Locate and identify every blood parasite.
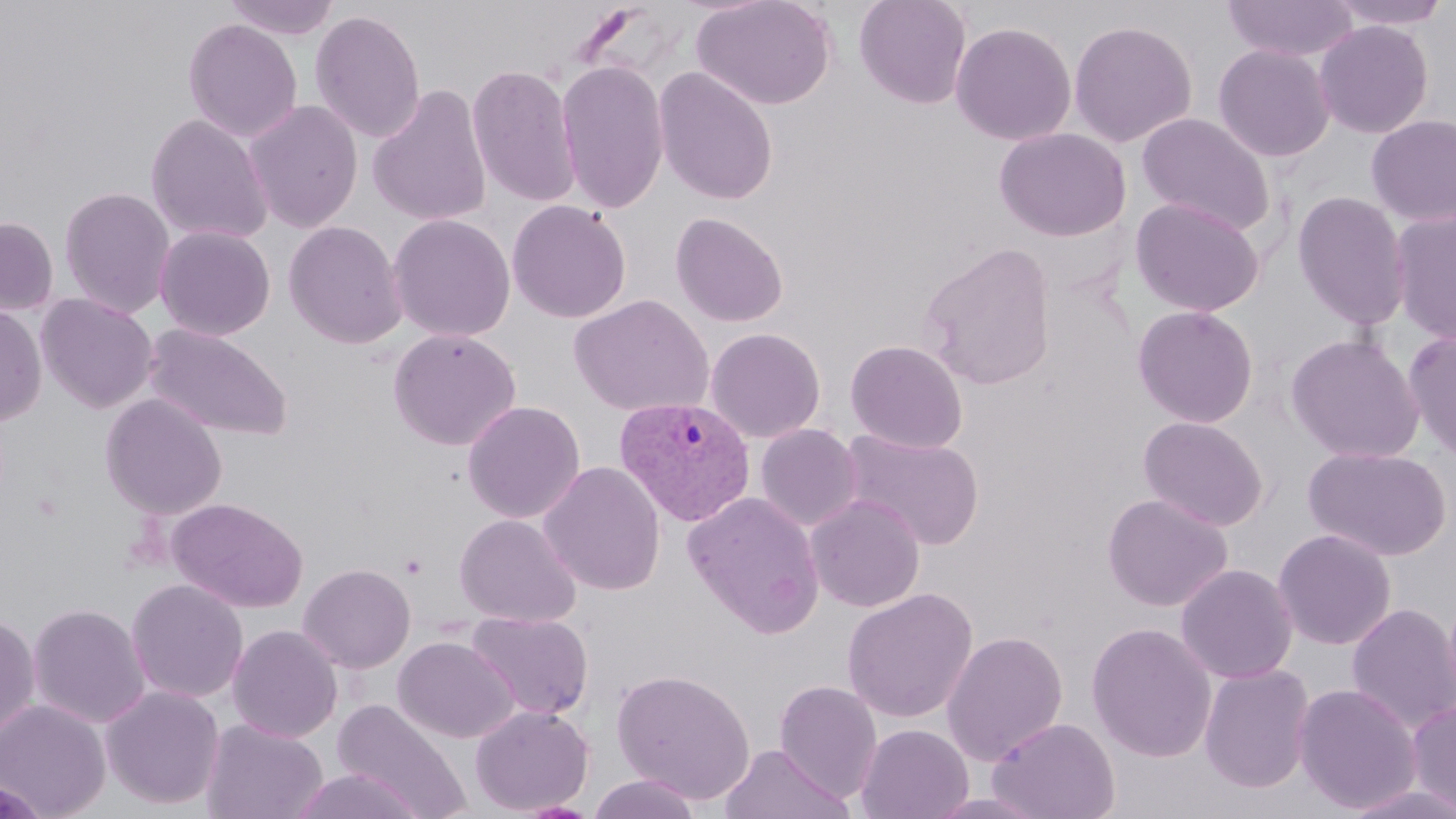

Approximate bounding boxes as (x1, y1, x2, y2) in pixels.
Plasmodium vivax-infected red blood cells: (614, 396, 756, 525).
No Plasmodium falciparum, Plasmodium ovale, Plasmodium malariae, Babesia divergens, or Trypanosoma brucei observed.

slide-level diagnosis = Plasmodium vivax
image size = 1456×819 pixels
preparation = thin blood smear
uninfected red blood cell locations = approximate bounding boxes as (x1, y1, x2, y2) in pixels: (223, 0, 342, 40), (691, 0, 837, 111), (853, 0, 973, 109), (1221, 0, 1359, 63), (1326, 0, 1454, 31), (310, 9, 426, 144), (182, 18, 303, 143), (1068, 19, 1198, 148), (1313, 19, 1434, 138), (950, 21, 1077, 145), (1212, 43, 1336, 163), (555, 60, 669, 215), (466, 63, 581, 209), (653, 67, 778, 205), (366, 84, 492, 227), (243, 99, 364, 233), (1137, 112, 1276, 235), (145, 114, 274, 245), (1365, 114, 1456, 227), (994, 127, 1131, 242), (59, 185, 176, 318), (1292, 190, 1412, 331), (1130, 197, 1266, 317), (507, 200, 631, 323), (1390, 208, 1456, 345), (670, 212, 789, 327), (388, 214, 515, 342), (0, 216, 58, 316), (283, 220, 408, 349), (154, 224, 276, 341), (917, 241, 1057, 390), (36, 293, 159, 413), (569, 294, 714, 417), (0, 303, 47, 426), (1132, 304, 1259, 428), (144, 324, 293, 441), (705, 327, 826, 443), (387, 328, 522, 451), (1402, 329, 1456, 465), (1285, 333, 1425, 464), (845, 340, 968, 453), (99, 393, 227, 519), (462, 400, 585, 523), (1138, 415, 1269, 532), (755, 423, 863, 531), (840, 429, 985, 550), (1302, 445, 1453, 561), (538, 461, 666, 596), (683, 492, 825, 637), (1102, 493, 1232, 612), (806, 494, 925, 612), (168, 497, 308, 613), (453, 513, 582, 628), (1272, 528, 1397, 651), (298, 563, 416, 673), (1175, 563, 1298, 684), (126, 579, 249, 704), (841, 588, 979, 723), (1346, 602, 1456, 733), (27, 603, 150, 728), (0, 611, 40, 744), (466, 611, 594, 721), (1086, 622, 1217, 762), (227, 624, 343, 742), (941, 630, 1068, 765), (392, 636, 519, 743), (1198, 663, 1315, 794), (612, 668, 756, 804), (774, 680, 884, 802), (1294, 683, 1422, 814), (100, 685, 225, 810), (1407, 697, 1456, 816), (0, 698, 111, 818), (332, 699, 470, 818), (469, 704, 594, 815), (986, 716, 1121, 819), (202, 718, 327, 819), (856, 724, 974, 819), (719, 744, 854, 819), (290, 768, 426, 819), (587, 775, 704, 819), (1342, 783, 1456, 819), (920, 791, 1054, 819), (510, 801, 601, 818)
modality = light microscopy
field of view = single
magnification = 1000x
stain = May-Grünwald-Giemsa
platelet locations = approximate bounding boxes as (x1, y1, x2, y2) in pixels: (400, 553, 428, 579)